Report the malaria status of this cell.
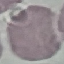

Uninfected.

Summary:
  - Capture: smartphone camera at the microscope eyepiece
  - Image type: cell patch, automatically extracted from a larger field of view and resized to 64 × 64 pixels
  - Preparation: thin blood film
  - Stain: Giemsa